Locate every P. falciparum parasite and give its life-cycle stage, and locate every leukocyte and any debris.
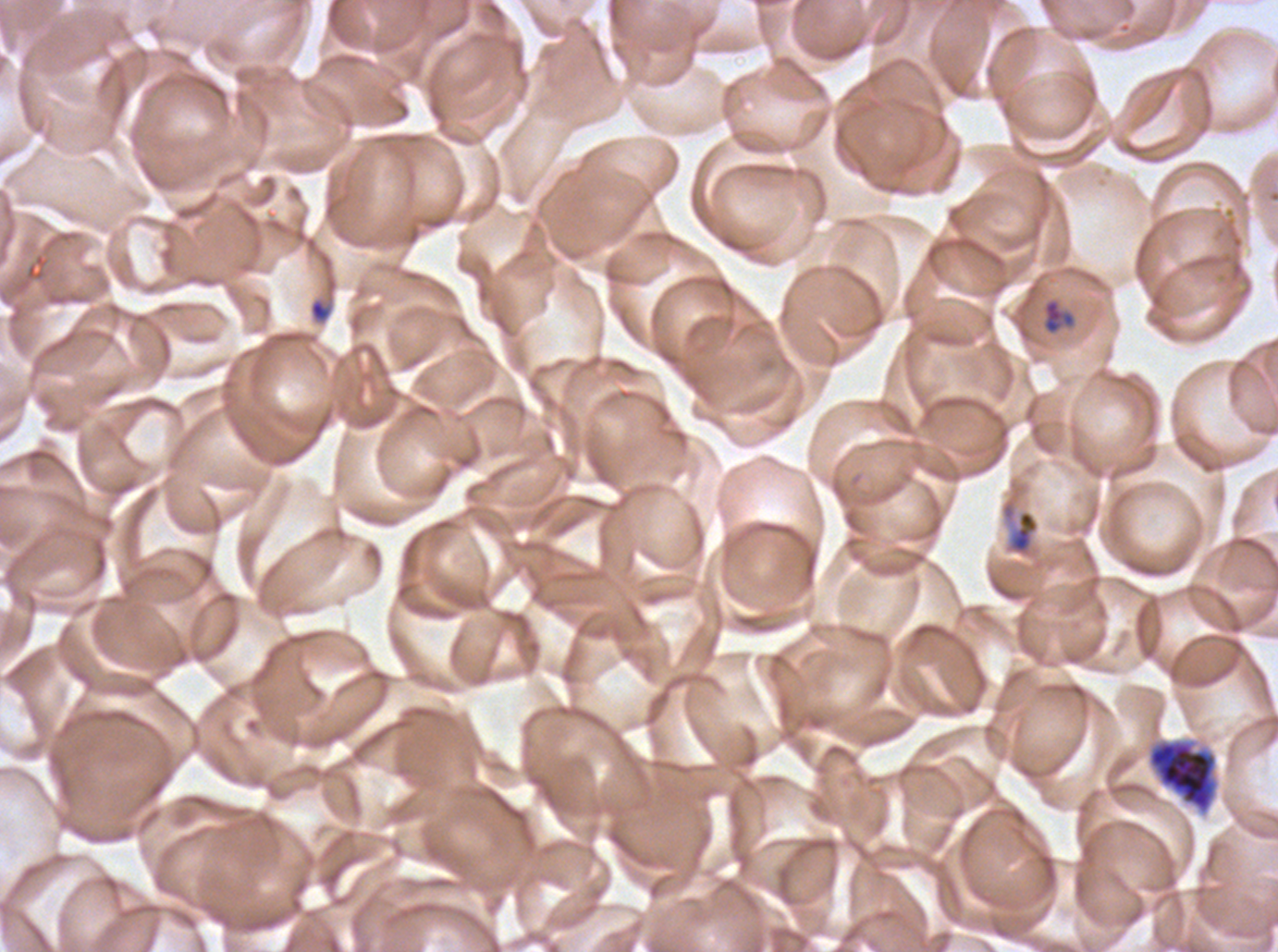

Approximate bounding boxes as (x1, y1, x2, y2) in pixels.
Rings: (308, 298, 332, 323), (1043, 299, 1075, 334).
Late-ring/early-trophozoite forms: (1000, 497, 1040, 558).
Late schizonts: (1147, 738, 1219, 814).
No mid trophozoites, late trophozoites, early schizonts, segmenters, gametocytes, leukocytes, or debris observed.

Summary:
  - Field of view: sub-image separated from a larger composite
  - Stain: Giemsa
  - Preparation: thin blood smear
  - Life-cycle stages observed: ring, late-ring/early-trophozoite, late schizont
  - Specimen: P. falciparum cultured ex vivo for 24 to 48 hours, from a patient in The Gambia
  - Image size: 1278×952 pixels